Identify the cell.
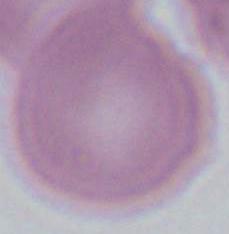
An erythrocyte.

Summary:
  - Modality: micrograph
  - Magnification: 1000x